Outline each Plasmodium ovale-infected red blood cell.
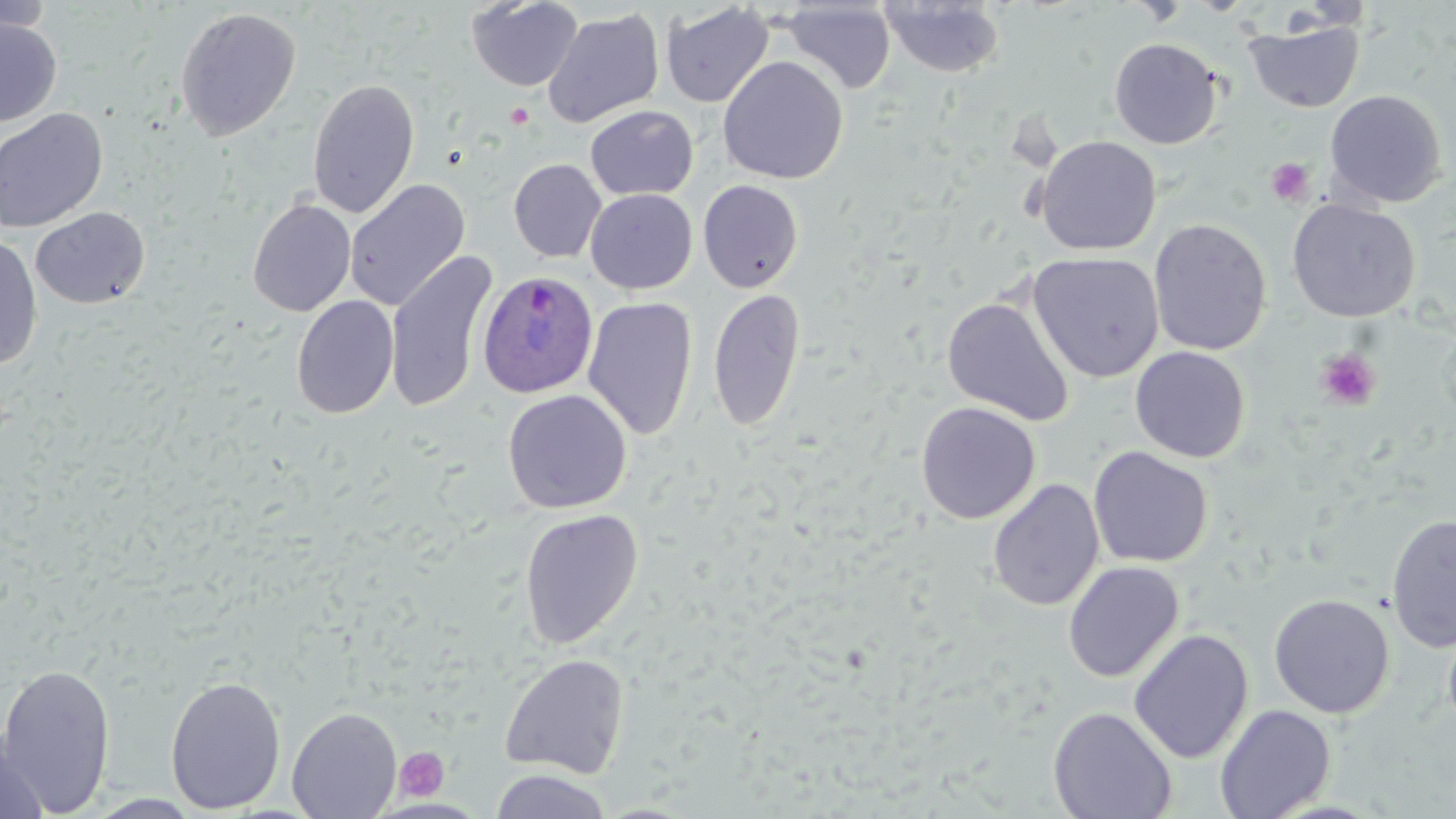

Approximate bounding boxes as [x1, y1, x2, y2] in pixels.
Plasmodium ovale-infected red blood cells: [477, 270, 599, 397].

Platelet locations: [1266, 158, 1315, 206], [1314, 348, 1382, 411], [394, 746, 449, 802]. Uninfected red blood cell locations: [0, 0, 57, 36], [466, 0, 583, 92], [878, 1, 1005, 78], [659, 2, 773, 109], [779, 2, 897, 94], [174, 7, 302, 141], [542, 8, 664, 128], [0, 18, 61, 127], [1244, 18, 1364, 112], [1109, 37, 1223, 149], [717, 56, 849, 184], [307, 78, 420, 219], [1325, 89, 1448, 208], [585, 105, 698, 200], [0, 108, 108, 232], [1035, 135, 1161, 255], [509, 159, 606, 263], [344, 179, 470, 311], [698, 179, 803, 293], [585, 189, 698, 294], [247, 198, 356, 317], [1287, 199, 1420, 322], [30, 207, 150, 309], [1149, 218, 1272, 356], [0, 235, 42, 372], [385, 250, 499, 414], [1027, 251, 1164, 383], [707, 288, 806, 432], [291, 295, 399, 419], [941, 295, 1074, 426], [582, 297, 698, 440], [1130, 345, 1250, 463], [502, 389, 632, 513], [916, 402, 1040, 524], [1088, 446, 1213, 568], [987, 479, 1105, 611], [519, 508, 644, 649], [1386, 513, 1456, 652], [1062, 561, 1184, 682], [1268, 594, 1394, 718], [1442, 616, 1456, 739], [1128, 629, 1253, 763], [498, 653, 630, 779], [0, 662, 116, 815], [165, 675, 287, 814], [1215, 704, 1336, 818], [1047, 706, 1177, 819], [287, 707, 402, 818], [0, 733, 52, 819], [489, 769, 613, 819]. Slide-level diagnosis: Plasmodium ovale. 1000x magnification. Thin blood film. Single field of view. May-Grünwald-Giemsa-stained preparation. Image is 1456×819 pixels. Optical microscopy.